Comment on the morphology of the red blood cells.
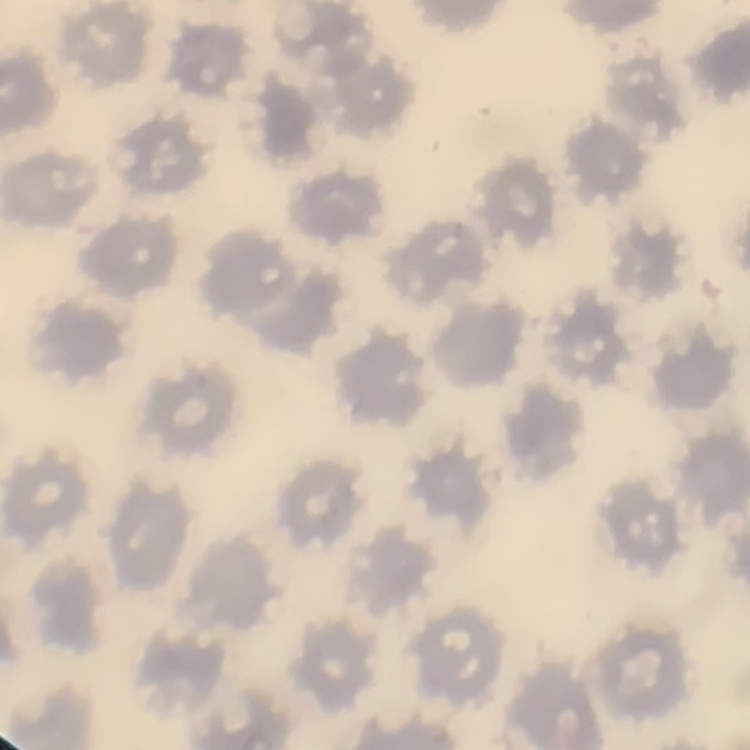
No rouleaux formation.

stain: Field's or Giemsa
image_type: one tile cut from a larger photomicrograph
preparation: thin blood film